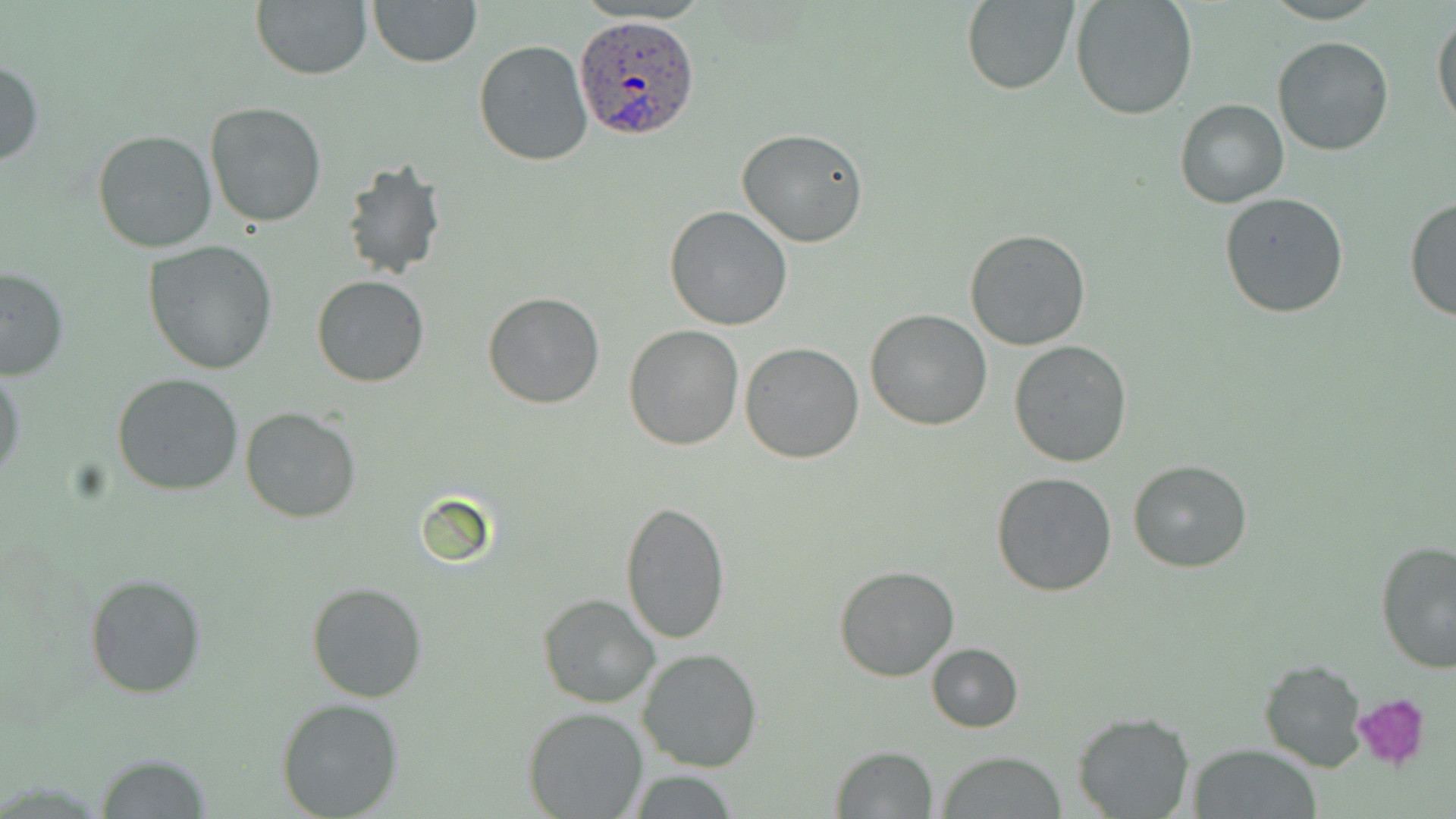
Approximate bounding boxes as (x1,y1)-(x2,y2) corner pairs in pixels. Uninfected red blood cell locations: (251,0)-(374,80), (368,0)-(482,67), (960,0)-(1078,95), (1070,0)-(1199,120), (1431,13)-(1455,132), (1272,35)-(1394,156), (473,40)-(595,168), (0,58)-(43,168), (1174,98)-(1289,209), (205,101)-(327,227), (736,128)-(870,248), (92,129)-(217,253), (341,158)-(446,281), (1219,192)-(1349,317), (1405,195)-(1456,325), (664,205)-(794,331), (965,229)-(1091,350), (143,242)-(278,374), (0,267)-(70,381), (312,274)-(429,387), (482,292)-(604,409), (865,308)-(994,430), (624,325)-(744,449), (1009,340)-(1132,467), (739,344)-(865,463), (1,368)-(24,485), (112,373)-(243,496), (240,408)-(361,524), (1127,459)-(1253,572), (989,471)-(1117,597), (619,501)-(732,645), (1375,540)-(1456,673), (833,564)-(961,682), (83,572)-(205,700), (307,581)-(427,703), (538,593)-(660,708), (926,643)-(1023,732), (638,648)-(762,771), (1258,659)-(1368,771), (277,699)-(405,818), (524,706)-(648,819), (1073,711)-(1195,817), (830,745)-(938,818), (1189,745)-(1324,818), (937,751)-(1068,818), (95,753)-(213,818). Plasmodium ovale-infected red blood cell locations: (573,15)-(702,142). Platelet locations: (1351,695)-(1431,772). Slide-level diagnosis: Plasmodium ovale. May-Grünwald-Giemsa-stained preparation. Light microscopy. Captured at 1000x magnification. Thin blood smear. Image is 1456×819 pixels. One field of a larger specimen.